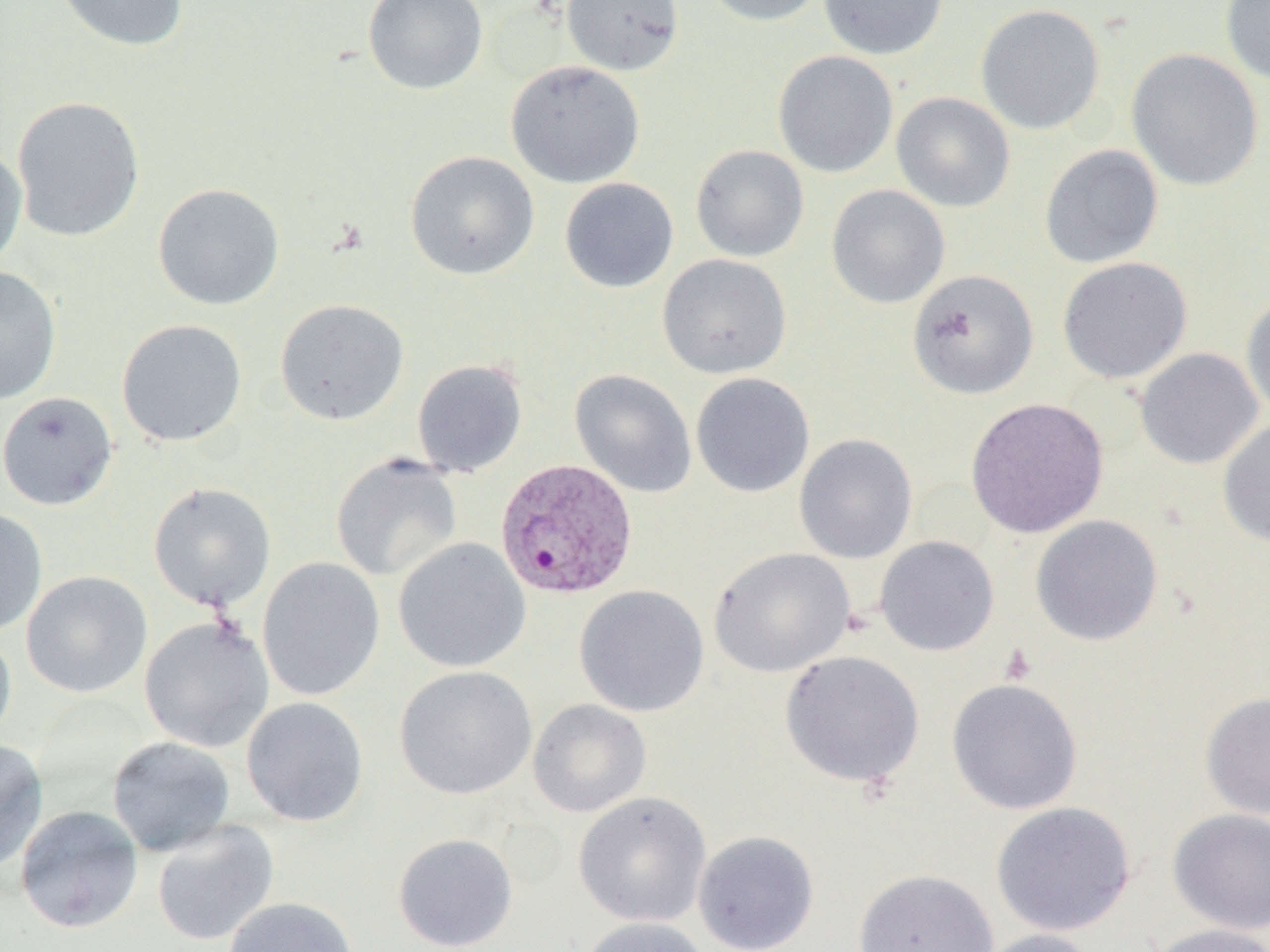
slide-level diagnosis = Plasmodium vivax
modality = optical microscopy
image size = 1270×952 pixels
magnification = 1000x
field of view = one of a larger specimen
platelet locations = approximate bounding boxes as (x1,y1)-(x2,y2) corner pairs in pixels: (998,643)-(1037,686)
Plasmodium vivax-infected red blood cell locations = approximate bounding boxes as (x1,y1)-(x2,y2) corner pairs in pixels: (495,458)-(638,601)
preparation = thin blood film
uninfected red blood cell locations = approximate bounding boxes as (x1,y1)-(x2,y2) corner pairs in pixels: (52,0)-(190,52), (363,0)-(489,94), (561,0)-(684,76), (698,0)-(826,26), (818,0)-(948,60), (1220,0)-(1270,84), (975,4)-(1106,135), (1126,48)-(1265,192), (772,50)-(899,178), (505,60)-(645,189), (891,92)-(1016,213), (11,96)-(146,242), (0,143)-(28,273), (1039,144)-(1164,269), (690,145)-(809,262), (405,150)-(540,281), (559,177)-(679,293), (152,183)-(285,310), (826,184)-(950,309), (657,254)-(792,379), (1057,257)-(1192,384), (0,266)-(62,405), (907,269)-(1039,400), (1241,291)-(1270,421), (275,299)-(409,425), (116,318)-(247,446), (1134,347)-(1264,470), (412,359)-(528,478), (570,369)-(697,498), (690,372)-(815,498), (0,391)-(118,511), (965,397)-(1109,538), (1217,419)-(1270,547), (794,433)-(918,563), (330,453)-(463,582), (147,482)-(277,611), (0,507)-(48,637), (1030,514)-(1164,646), (874,535)-(999,656), (393,538)-(531,673), (709,547)-(855,678), (256,557)-(386,702), (21,570)-(152,698), (574,584)-(709,717), (139,616)-(274,753), (0,627)-(17,746), (779,650)-(925,789), (394,666)-(538,800), (946,677)-(1083,815), (1200,691)-(1270,820), (241,697)-(369,827), (527,699)-(652,817), (106,736)-(236,857), (0,739)-(49,873), (572,791)-(712,927), (990,801)-(1137,936), (15,805)-(144,934), (1166,807)-(1270,934), (151,820)-(279,947), (693,829)-(820,952), (392,832)-(518,952), (853,868)-(999,952), (223,897)-(360,952), (575,916)-(714,952), (1144,923)-(1269,952), (970,928)-(1103,952)